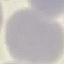
result: negative for malaria parasites
stain: Giemsa
preparation: thin blood smear
image_type: automatically extracted cell patch, resized to 64 × 64 pixels
capture: smartphone camera at the microscope eyepiece